Assess this cell for malaria.
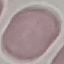

It is uninfected.

stain: Giemsa
image_type: cell patch, automatically extracted from a larger field of view and resized to 64 × 64 pixels
preparation: thin smear
capture: smartphone camera at the microscope eyepiece